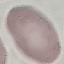

Summary:
  - Malaria status: uninfected
  - Preparation: thin smear
  - Image type: automatically extracted cell patch, resized to 64 × 64 pixels
  - Stain: Giemsa
  - Capture: smartphone camera at the microscope eyepiece